Comment on the morphology of the erythrocytes.
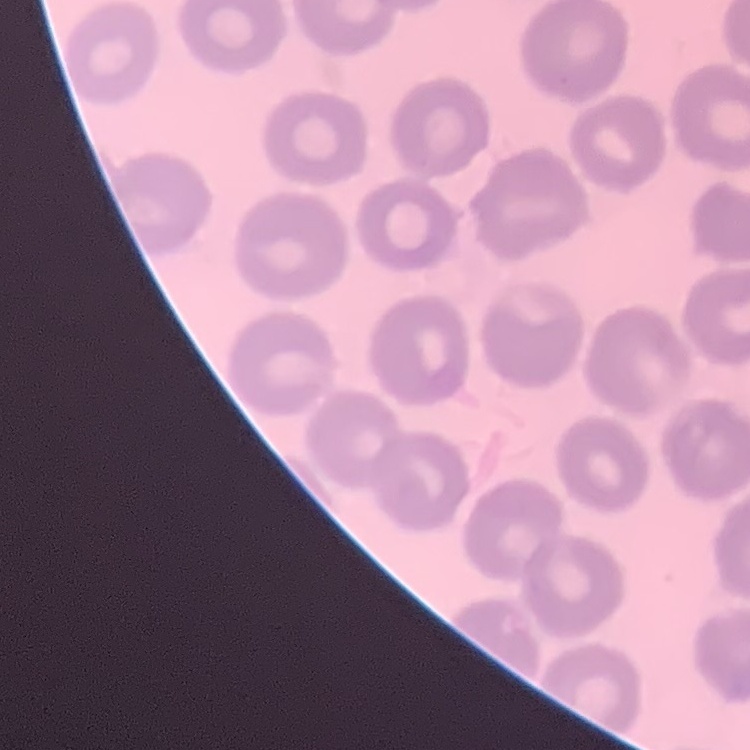

No rouleaux formation.

Stained with either Field's or Giemsa. Thin peripheral smear. One tile cut from a larger photomicrograph.